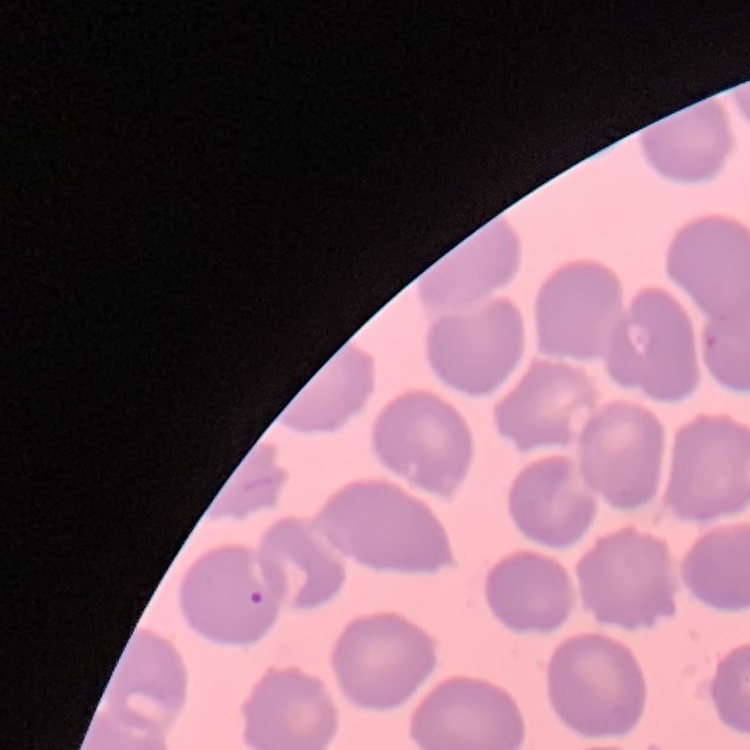
Summary:
  - Erythrocyte morphology: no rouleaux formation
  - Stain: Field's or Giemsa
  - Image type: square crop of a larger photomicrograph
  - Preparation: thin peripheral smear